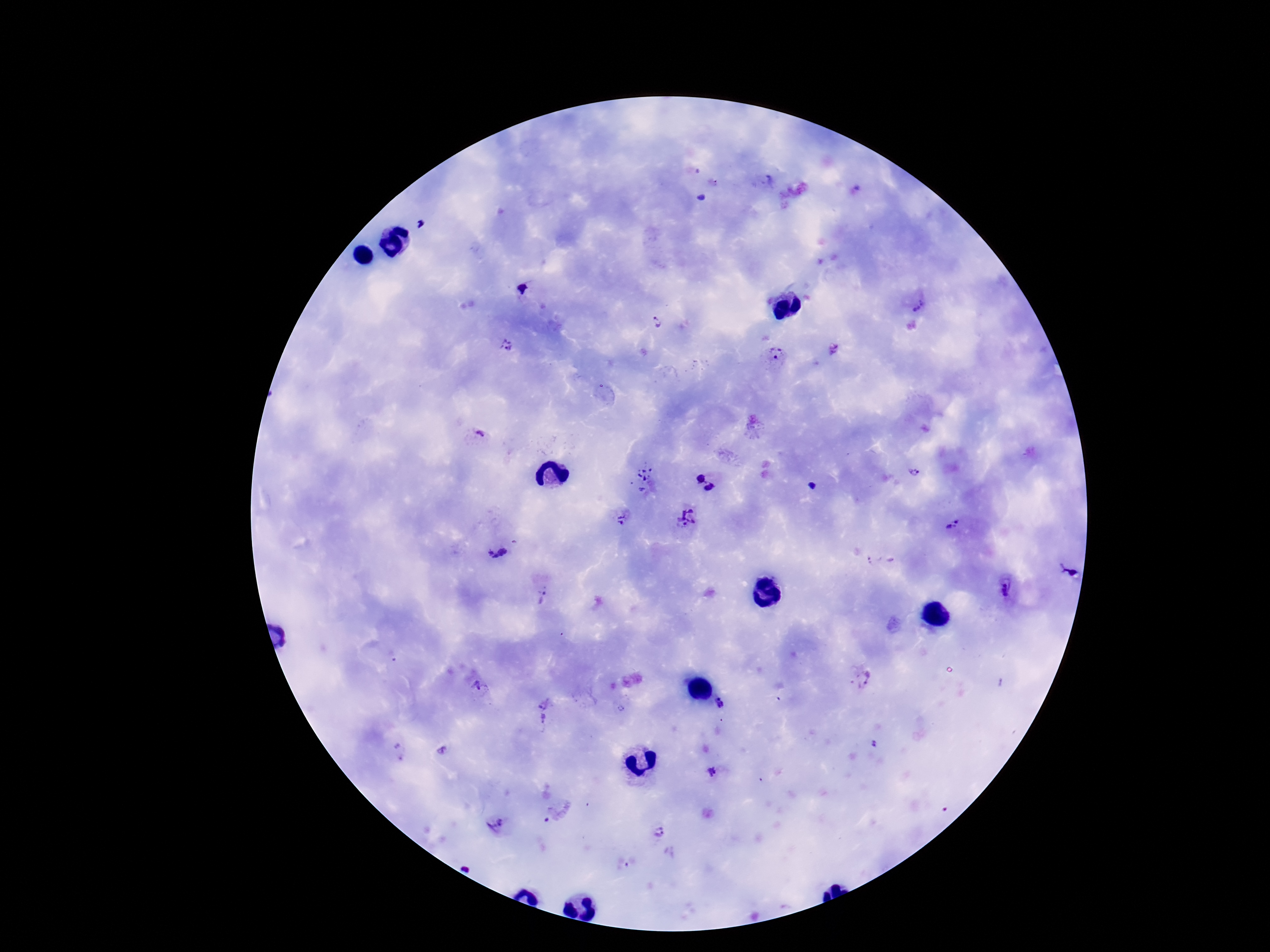

{
  "image_size": "1270×952 pixels",
  "plasmodium_parasite_locations": "approximate centers as [x, y] in pixels: [918, 303], [657, 323], [506, 345], [834, 348], [776, 353], [479, 436], [916, 475], [646, 477], [701, 478], [711, 488], [624, 516], [688, 518], [953, 527], [497, 552], [880, 560], [1068, 570], [1004, 591], [544, 594], [861, 678], [477, 688], [544, 701], [721, 703], [621, 709], [543, 719], [874, 744], [442, 751], [401, 752], [713, 775], [496, 825], [660, 831]",
  "stain": "Giemsa",
  "patient_malaria_status": "infected",
  "preparation": "thick blood film",
  "magnification": "100x",
  "capture": "smartphone camera through the microscope eyepiece",
  "field_of_view": "single"
}